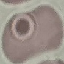 Result: no malaria parasites seen. Giemsa stain. Cell patch, automatically extracted from a larger field of view and resized to 64 × 64 pixels. Photographed with a smartphone camera at the microscope eyepiece. Thin blood smear.